Identify the parasite.
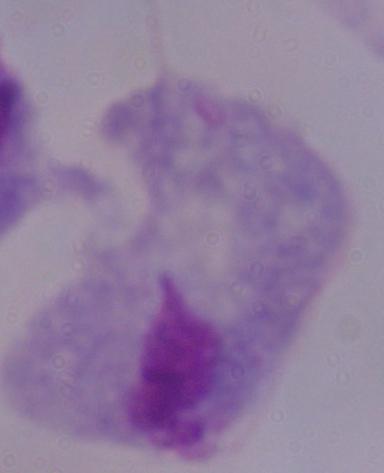
A trichomonad.

magnification = 1000x
modality = micrograph